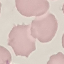

Malaria status: uninfected. Automatically extracted cell patch, resized to 64 × 64 pixels. Photographed with a smartphone camera at the microscope eyepiece. Giemsa-stained preparation. Thin smear of blood.